Give the position of each P. falciparum parasite with its life-cycle stage, each leukocyte, and any debris.
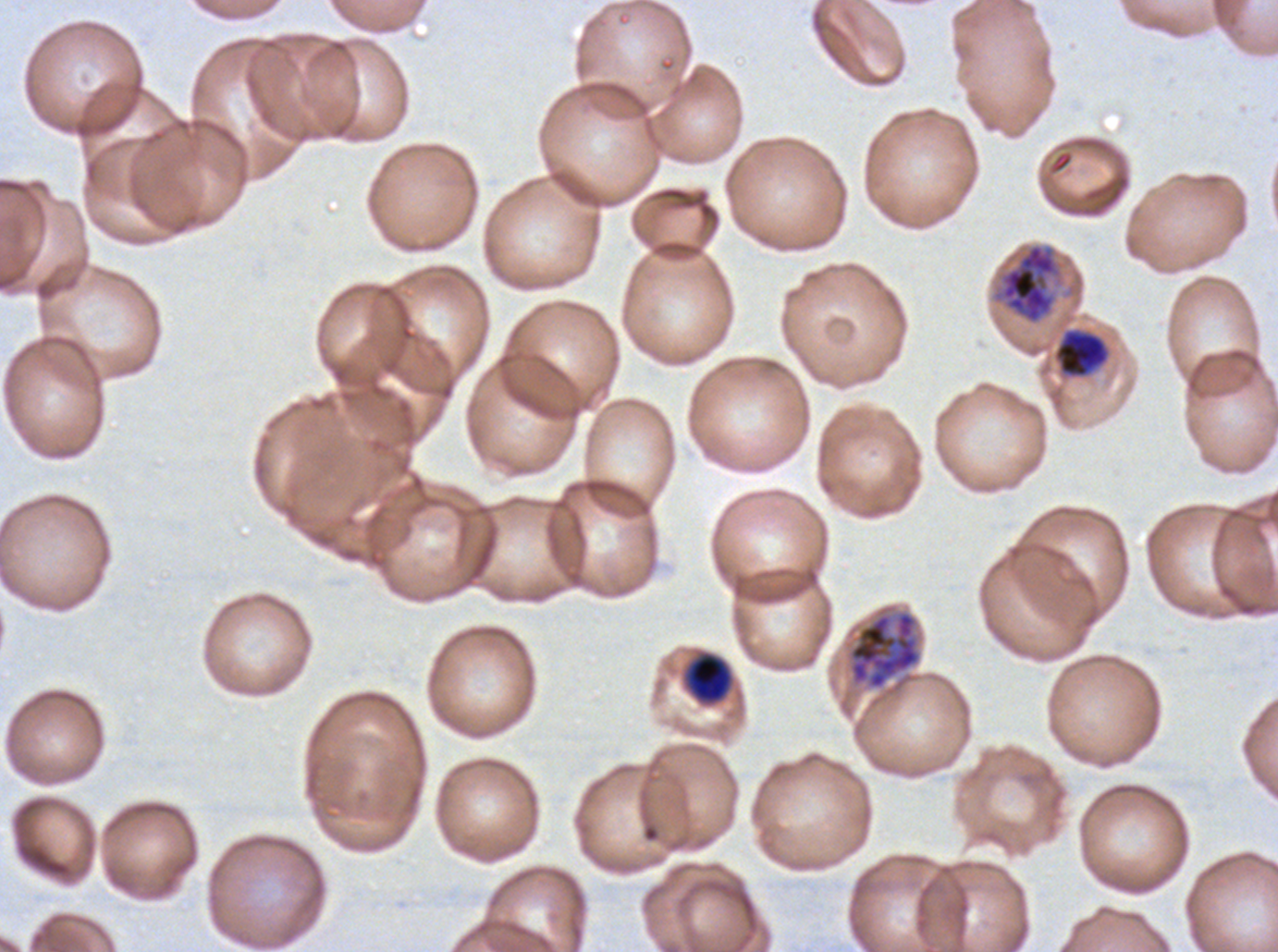
Approximate bounding boxes as (x1, y1, x2, y2) in pixels.
Mid trophozoites: (1054, 329, 1109, 378), (685, 653, 733, 704).
Early schizonts: (990, 242, 1066, 326), (847, 609, 922, 690).
No rings, late-ring/early-trophozoite forms, late trophozoites, late schizonts, segmenters, gametocytes, leukocytes, or debris observed.

Giemsa stain. One sub-image of a larger composite. Life-cycle stages observed: mid trophozoite, early schizont. P. falciparum from a patient in The Gambia, cultured ex vivo for 24 to 48 hours. Thin blood smear. Image is 1278×952 pixels.